Report the malaria status of this cell.
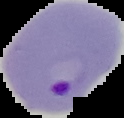
It is parasitized.

image size = 124×118 pixels
preparation = thin blood film
image type = segmented cell region on a black background